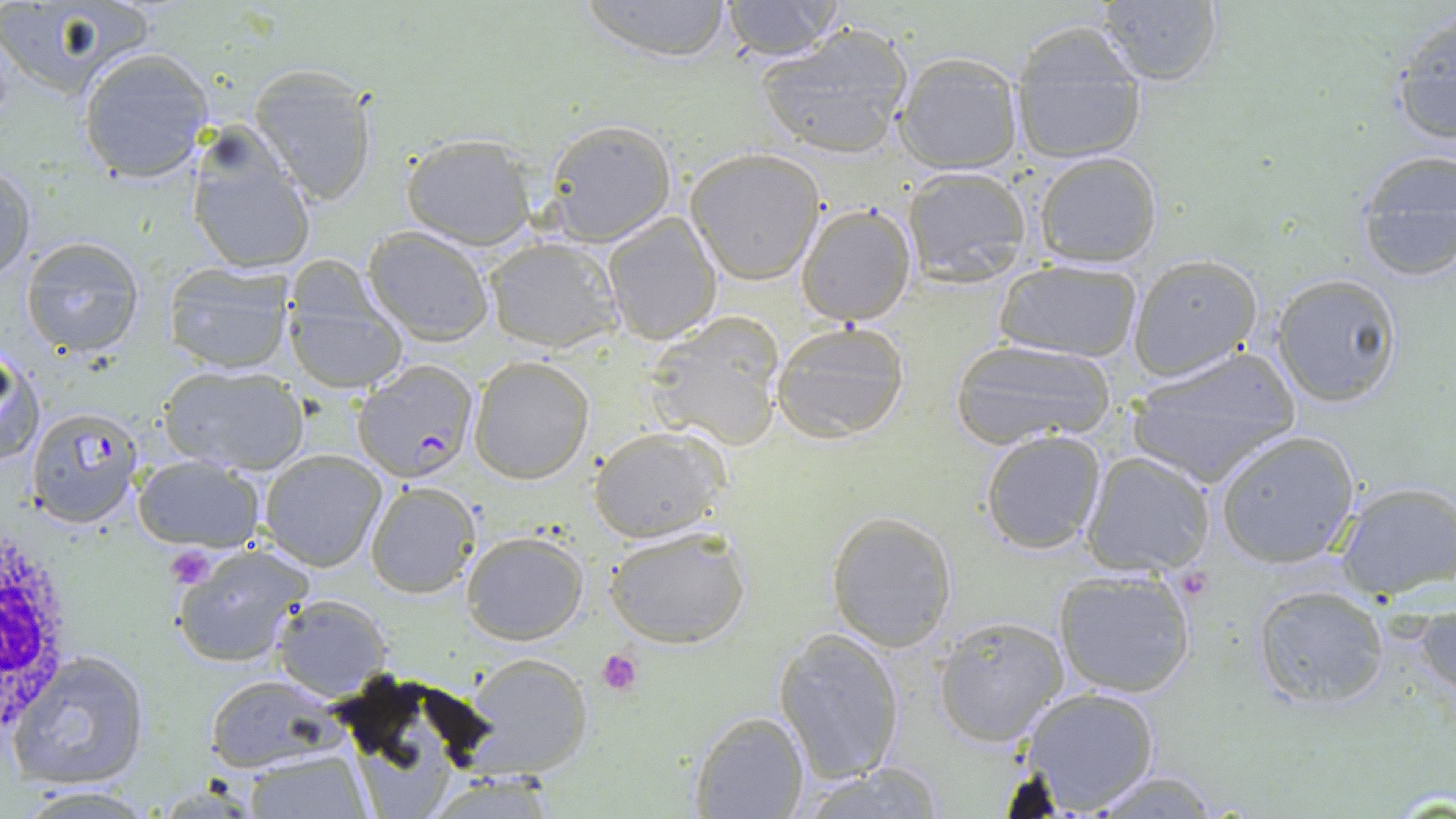

slide_level_diagnosis: Plasmodium falciparum
magnification: 1000x
uninfected_red_blood_cell_locations: 'approximate bounding boxes as (x1, y1, x2, y2) in pixels: (576, 0, 738, 63), (717, 0, 848, 61), (1094, 0, 1223, 88), (0, 1, 159, 106), (732, 1, 890, 109), (1388, 13, 1455, 150), (756, 25, 916, 158), (1009, 25, 1148, 167), (79, 48, 213, 183), (894, 54, 1024, 174), (249, 64, 379, 205), (542, 119, 676, 245), (184, 129, 317, 277), (401, 132, 536, 249), (685, 148, 826, 284), (1033, 151, 1162, 269), (1351, 151, 1456, 285), (1, 162, 36, 284), (901, 166, 1033, 285), (797, 202, 917, 325), (603, 213, 721, 343), (363, 227, 495, 345), (484, 236, 623, 354), (19, 237, 145, 356), (1126, 254, 1262, 381), (162, 259, 296, 376), (996, 260, 1142, 364), (285, 269, 409, 393), (1271, 272, 1403, 408), (646, 318, 783, 451), (770, 319, 912, 442), (951, 336, 1114, 448), (2, 347, 43, 466), (1126, 347, 1302, 488), (468, 355, 596, 484), (158, 365, 307, 476), (589, 425, 731, 543), (980, 429, 1109, 556), (1215, 430, 1361, 568), (260, 448, 387, 571), (1079, 452, 1215, 578), (135, 454, 264, 552), (1333, 480, 1456, 602), (365, 481, 480, 598), (826, 511, 959, 651), (604, 525, 751, 647), (462, 532, 588, 644), (172, 541, 313, 668), (1052, 568, 1198, 699), (1252, 584, 1390, 707), (272, 593, 393, 698), (1416, 593, 1456, 704), (935, 615, 1069, 746), (773, 628, 907, 784), (9, 649, 152, 789), (464, 656, 590, 781), (203, 673, 338, 771), (1018, 685, 1161, 815), (690, 709, 809, 818), (358, 717, 446, 818), (241, 749, 370, 818), (795, 762, 946, 818), (436, 770, 554, 819), (1084, 770, 1225, 818), (11, 783, 164, 816)'
stain: May-Grünwald-Giemsa
image_size: 1456×819 pixels
white_blood_cell_locations: 'approximate bounding boxes as (x1, y1, x2, y2) in pixels: (0, 522, 77, 739)'
plasmodium_falciparum_infected_red_blood_cell_locations: 'approximate bounding boxes as (x1, y1, x2, y2) in pixels: (352, 359, 479, 481), (25, 409, 145, 529)'
modality: optical microscopy
field_of_view: one of a larger specimen
platelet_locations: 'approximate bounding boxes as (x1, y1, x2, y2) in pixels: (166, 546, 215, 589), (597, 650, 642, 696)'
preparation: thin blood film